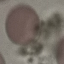

result = negative for malaria parasites
preparation = thin smear
image type = automatically extracted cell patch, resized to 64 × 64 pixels
stain = Giemsa
capture = smartphone camera at the microscope eyepiece